Outline each P. falciparum parasite and classify it by life-cycle stage.
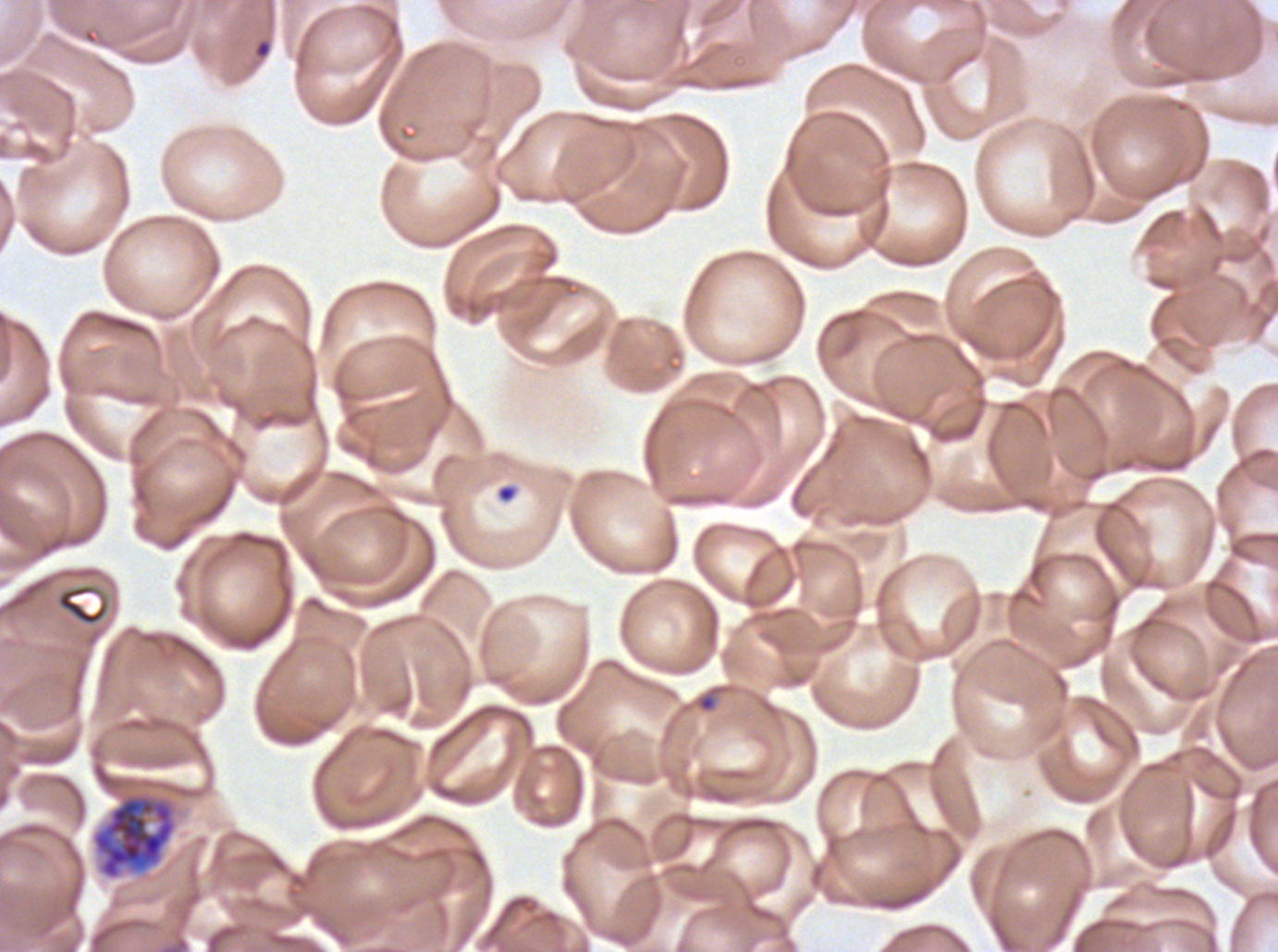
Approximate bounding boxes as (x1, y1, x2, y2) in pixels.
Rings: (253, 38, 272, 59), (495, 483, 519, 504), (696, 692, 717, 713).
Early schizonts: (92, 794, 177, 880).
No late-ring/early-trophozoite forms, mid trophozoites, late trophozoites, late schizonts, segmenters, or gametocytes observed.

Debris locations: (55, 582, 111, 627). Life-cycle stages observed: ring, early schizont. Thin blood smear. Image is 1278×952 pixels. One sub-image of a larger composite. Ex-vivo P. falciparum culture from a patient in The Gambia, grown for 24 to 48 hours. Giemsa stain.